Name the cell type shown.
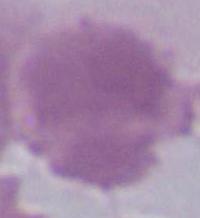

This is an erythrocyte.

modality = micrograph
magnification = 1000x